Point out each Plasmodium parasite.
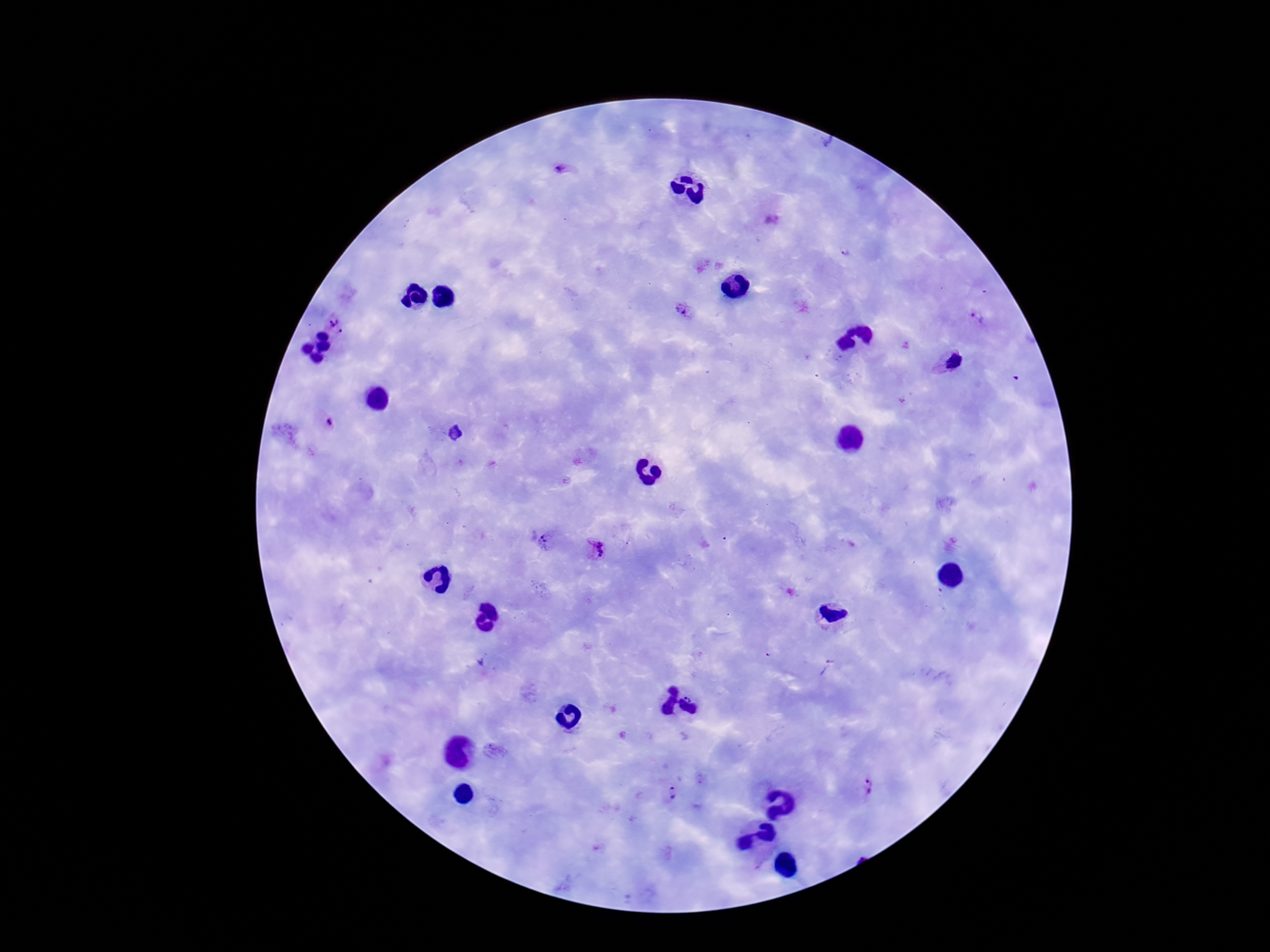
Approximate object centers, in pixels from the top-left corner.
Plasmodium parasites: (x=560, y=168), (x=772, y=220), (x=844, y=254), (x=683, y=309), (x=333, y=318), (x=977, y=318), (x=343, y=333), (x=952, y=362), (x=328, y=423), (x=455, y=433), (x=546, y=541), (x=597, y=550), (x=480, y=662), (x=829, y=667), (x=866, y=787), (x=672, y=794).

preparation = thick peripheral-blood smear
magnification = 100x
patient malaria status = infected
capture = smartphone camera through the microscope eyepiece
stain = Giemsa
image size = 1270×952 pixels
field of view = one from this slide